Name the blood parasite species.
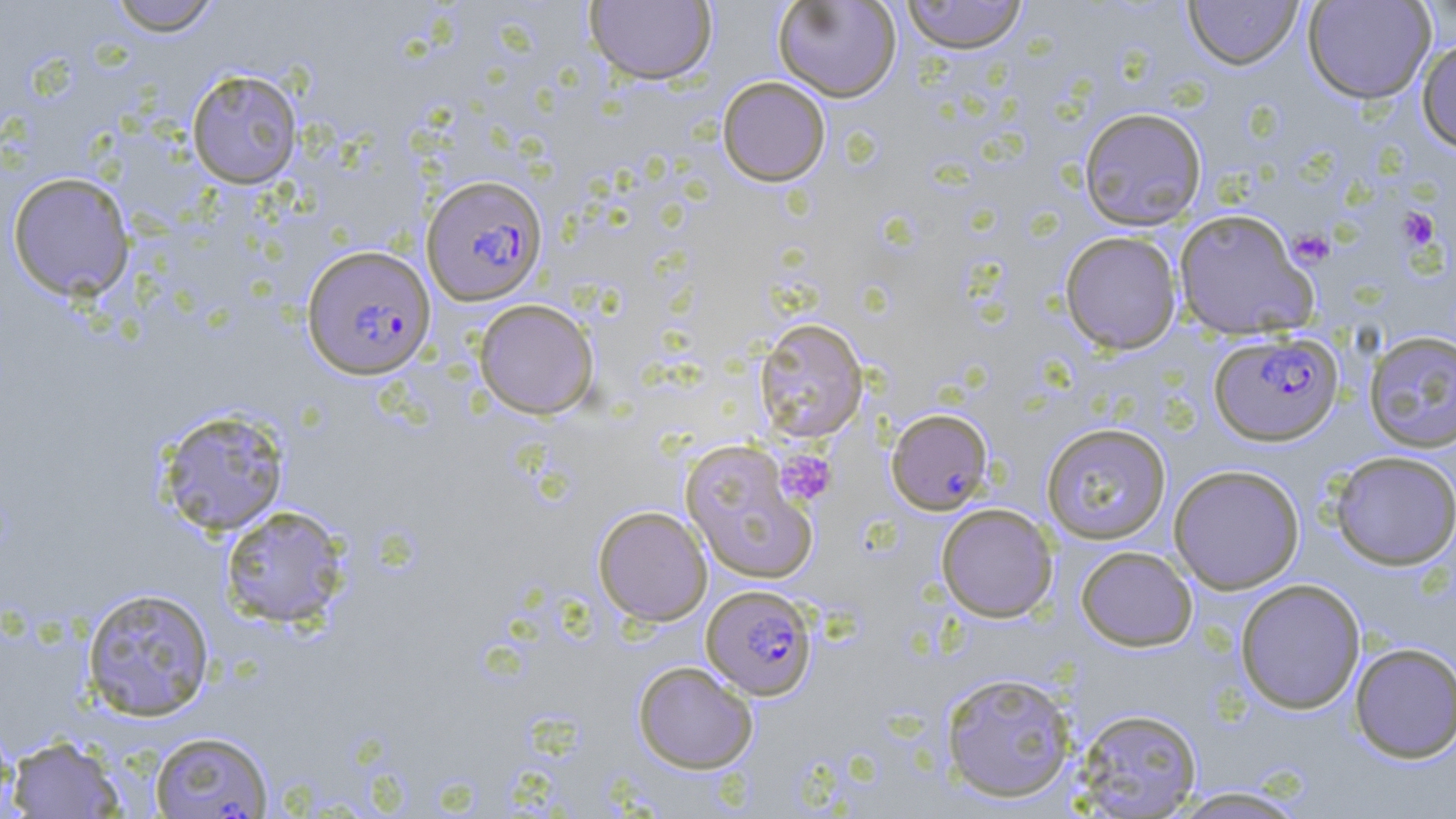
Plasmodium falciparum.

uninfected red blood cell locations (subset) = approximate bounding boxes as named x1/y1/x2/y2 corners in pixels: (x1=107, y1=0, x2=221, y2=36), (x1=584, y1=0, x2=717, y2=85), (x1=772, y1=0, x2=901, y2=102), (x1=1183, y1=0, x2=1304, y2=70), (x1=1302, y1=0, x2=1436, y2=104), (x1=900, y1=1, x2=1029, y2=54), (x1=1416, y1=36, x2=1456, y2=153), (x1=186, y1=69, x2=303, y2=189), (x1=717, y1=77, x2=831, y2=186), (x1=1078, y1=107, x2=1208, y2=231), (x1=6, y1=172, x2=135, y2=301), (x1=1172, y1=207, x2=1318, y2=340), (x1=1059, y1=231, x2=1182, y2=354), (x1=473, y1=298, x2=600, y2=419), (x1=753, y1=317, x2=868, y2=443), (x1=1363, y1=330, x2=1456, y2=453), (x1=156, y1=407, x2=290, y2=536), (x1=886, y1=408, x2=994, y2=515), (x1=1041, y1=422, x2=1172, y2=544), (x1=679, y1=440, x2=819, y2=585), (x1=1329, y1=451, x2=1456, y2=570), (x1=1168, y1=464, x2=1305, y2=594), (x1=935, y1=503, x2=1058, y2=622), (x1=219, y1=505, x2=350, y2=629), (x1=593, y1=506, x2=712, y2=626), (x1=1075, y1=545, x2=1198, y2=651), (x1=1234, y1=578, x2=1366, y2=714), (x1=80, y1=586, x2=216, y2=722), (x1=1349, y1=642, x2=1456, y2=763), (x1=632, y1=660, x2=758, y2=773), (x1=939, y1=671, x2=1078, y2=802), (x1=1073, y1=707, x2=1203, y2=817), (x1=0, y1=716, x2=20, y2=819), (x1=5, y1=734, x2=127, y2=818), (x1=1169, y1=786, x2=1311, y2=818)
magnification = 1000x
field of view = single
platelet locations = approximate bounding boxes as named x1/y1/x2/y2 corners in pixels: (x1=1398, y1=207, x2=1440, y2=251), (x1=1288, y1=229, x2=1334, y2=268), (x1=774, y1=449, x2=837, y2=507)
preparation = thin blood film
stain = May-Grünwald-Giemsa
Plasmodium falciparum-infected red blood cell locations (subset) = approximate bounding boxes as named x1/y1/x2/y2 corners in pixels: (x1=421, y1=174, x2=547, y2=306), (x1=301, y1=244, x2=436, y2=380), (x1=1209, y1=330, x2=1343, y2=446), (x1=701, y1=584, x2=818, y2=700)
image size = 1456×819 pixels
modality = optical microscopy